Assess for Plasmodium parasites.
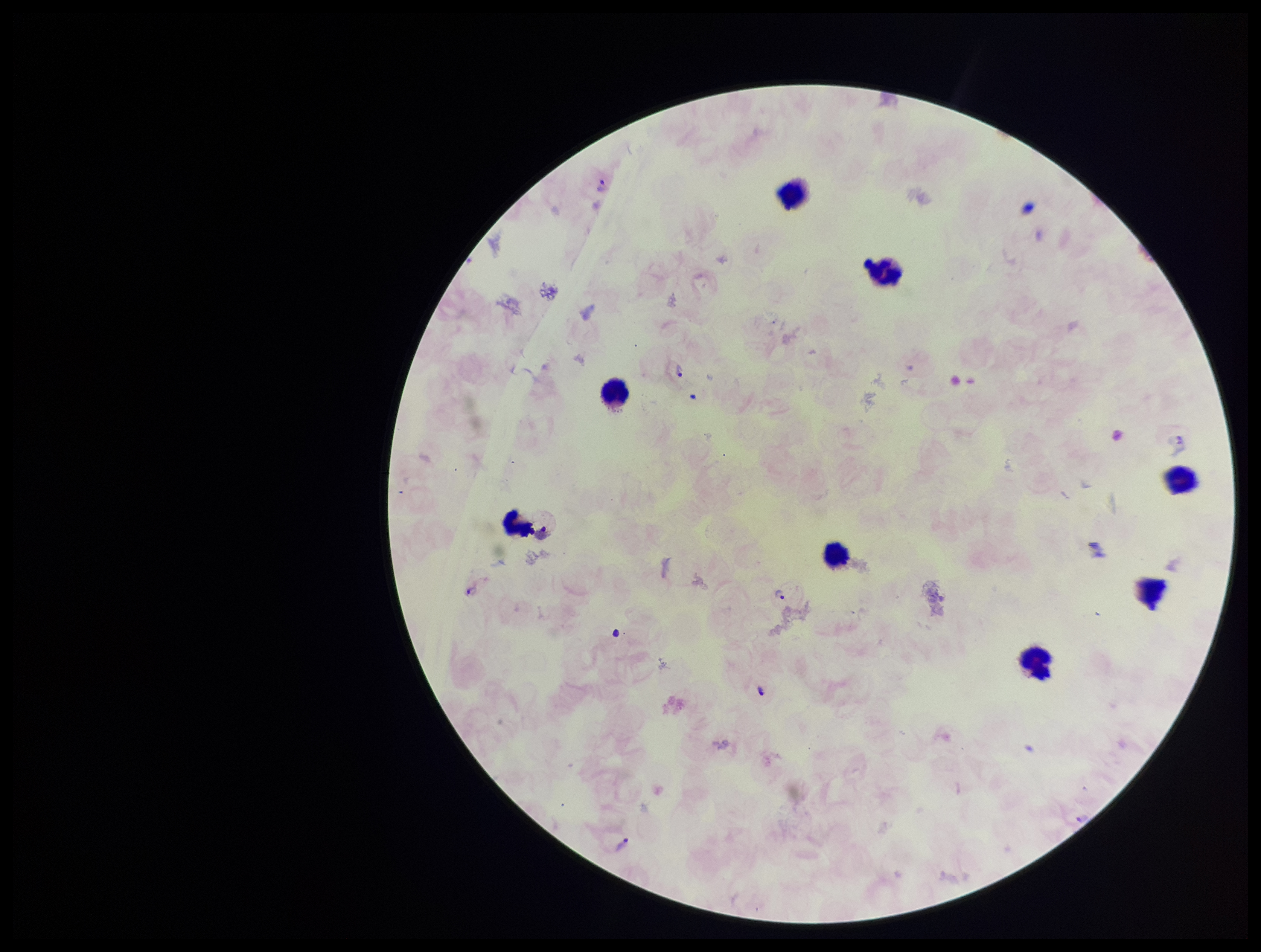

Detected.

Summary:
  - Leukocyte count: 8
  - Image size: 1261×952 pixels
  - Patient malaria status: infected
  - Capture: smartphone photograph through the microscope eyepiece
  - Preparation: thick blood smear
  - Species reported for this patient: Plasmodium vivax
  - Field of view: single
  - Stain: Giemsa
  - Parasite count: 4